Outline each blood parasite and name the species.
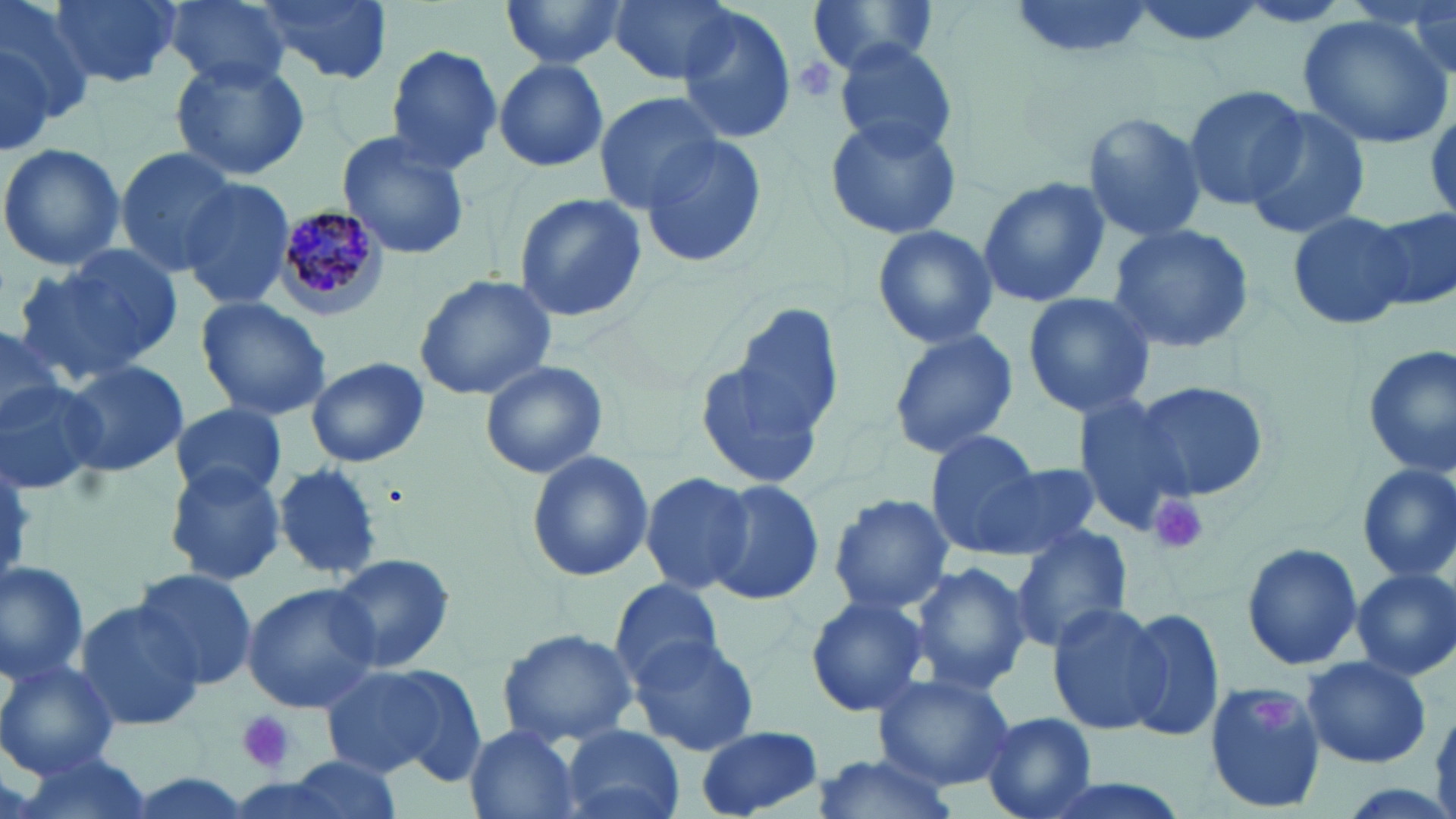
Approximate bounding boxes as named x1/y1/x2/y2 corners in pixels.
Plasmodium malariae-infected red blood cells: (x1=272, y1=205, x2=386, y2=324).
No Plasmodium falciparum, Plasmodium ovale, Plasmodium vivax, Babesia divergens, or Trypanosoma brucei observed.

Platelet locations: (x1=791, y1=57, x2=840, y2=107), (x1=1148, y1=495, x2=1207, y2=556), (x1=1252, y1=694, x2=1298, y2=734), (x1=236, y1=711, x2=295, y2=773). Uninfected red blood cell locations: (x1=0, y1=0, x2=96, y2=127), (x1=50, y1=0, x2=182, y2=89), (x1=160, y1=0, x2=292, y2=88), (x1=250, y1=0, x2=394, y2=87), (x1=499, y1=0, x2=627, y2=70), (x1=608, y1=0, x2=738, y2=85), (x1=805, y1=0, x2=943, y2=73), (x1=1010, y1=0, x2=1153, y2=66), (x1=1122, y1=0, x2=1268, y2=51), (x1=1235, y1=3, x2=1355, y2=29), (x1=676, y1=8, x2=797, y2=143), (x1=1403, y1=9, x2=1453, y2=80), (x1=1299, y1=17, x2=1451, y2=150), (x1=834, y1=39, x2=958, y2=155), (x1=385, y1=44, x2=505, y2=175), (x1=172, y1=55, x2=309, y2=181), (x1=494, y1=57, x2=611, y2=172), (x1=1182, y1=83, x2=1309, y2=211), (x1=593, y1=91, x2=725, y2=211), (x1=1242, y1=106, x2=1375, y2=240), (x1=1081, y1=111, x2=1208, y2=245), (x1=824, y1=115, x2=964, y2=241), (x1=335, y1=132, x2=472, y2=261), (x1=636, y1=133, x2=770, y2=269), (x1=0, y1=140, x2=125, y2=274), (x1=114, y1=148, x2=238, y2=278), (x1=978, y1=177, x2=1110, y2=310), (x1=178, y1=178, x2=296, y2=312), (x1=512, y1=194, x2=648, y2=322), (x1=1285, y1=208, x2=1416, y2=330), (x1=1368, y1=209, x2=1455, y2=312), (x1=1105, y1=224, x2=1256, y2=357), (x1=870, y1=225, x2=998, y2=350), (x1=14, y1=250, x2=178, y2=385), (x1=413, y1=275, x2=555, y2=399), (x1=1020, y1=291, x2=1157, y2=420), (x1=194, y1=296, x2=333, y2=421), (x1=728, y1=303, x2=844, y2=446), (x1=0, y1=323, x2=62, y2=438), (x1=886, y1=328, x2=1020, y2=460), (x1=695, y1=338, x2=831, y2=491), (x1=1361, y1=344, x2=1455, y2=476), (x1=305, y1=356, x2=429, y2=467), (x1=64, y1=359, x2=188, y2=480), (x1=479, y1=360, x2=607, y2=478), (x1=0, y1=375, x2=106, y2=497), (x1=1129, y1=379, x2=1272, y2=502), (x1=1071, y1=396, x2=1193, y2=534), (x1=169, y1=403, x2=291, y2=505), (x1=924, y1=431, x2=1051, y2=556), (x1=525, y1=451, x2=654, y2=581), (x1=976, y1=462, x2=1104, y2=557), (x1=1355, y1=463, x2=1455, y2=581), (x1=271, y1=464, x2=383, y2=580), (x1=165, y1=467, x2=286, y2=586), (x1=641, y1=471, x2=756, y2=594), (x1=706, y1=478, x2=826, y2=606), (x1=827, y1=494, x2=954, y2=615), (x1=1010, y1=523, x2=1133, y2=650), (x1=1241, y1=540, x2=1362, y2=671), (x1=327, y1=552, x2=455, y2=676), (x1=0, y1=557, x2=90, y2=685), (x1=909, y1=561, x2=1030, y2=695), (x1=1351, y1=569, x2=1456, y2=680), (x1=133, y1=570, x2=259, y2=690), (x1=607, y1=578, x2=726, y2=684), (x1=241, y1=582, x2=380, y2=714), (x1=805, y1=595, x2=929, y2=718), (x1=73, y1=599, x2=204, y2=735), (x1=1044, y1=603, x2=1170, y2=736), (x1=1121, y1=606, x2=1227, y2=744), (x1=16, y1=620, x2=168, y2=764), (x1=498, y1=627, x2=638, y2=748), (x1=629, y1=635, x2=762, y2=757), (x1=1299, y1=657, x2=1432, y2=767), (x1=0, y1=659, x2=119, y2=777), (x1=319, y1=663, x2=468, y2=780), (x1=873, y1=671, x2=1017, y2=790), (x1=1202, y1=682, x2=1325, y2=811), (x1=982, y1=712, x2=1099, y2=819), (x1=561, y1=725, x2=684, y2=819), (x1=695, y1=725, x2=827, y2=816), (x1=464, y1=727, x2=585, y2=819), (x1=14, y1=745, x2=150, y2=819), (x1=811, y1=752, x2=958, y2=819), (x1=281, y1=756, x2=407, y2=818), (x1=1022, y1=772, x2=1199, y2=819). Slide-level diagnosis: Plasmodium malariae. One field of a larger specimen. May-Grünwald-Giemsa stain. Thin blood film. Captured at 1000x magnification. Image is 1456×819 pixels. Optical microscopy.